Classify this cell by malaria status.
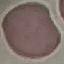
It is uninfected.

Summary:
  - Image type: automatically extracted cell patch, resized to 64 × 64 pixels
  - Capture: smartphone camera at the microscope eyepiece
  - Preparation: thin smear
  - Stain: Giemsa